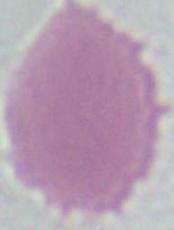

modality = photomicrograph
magnification = 1000x
identification = red blood cell